Point out every Plasmodium parasite.
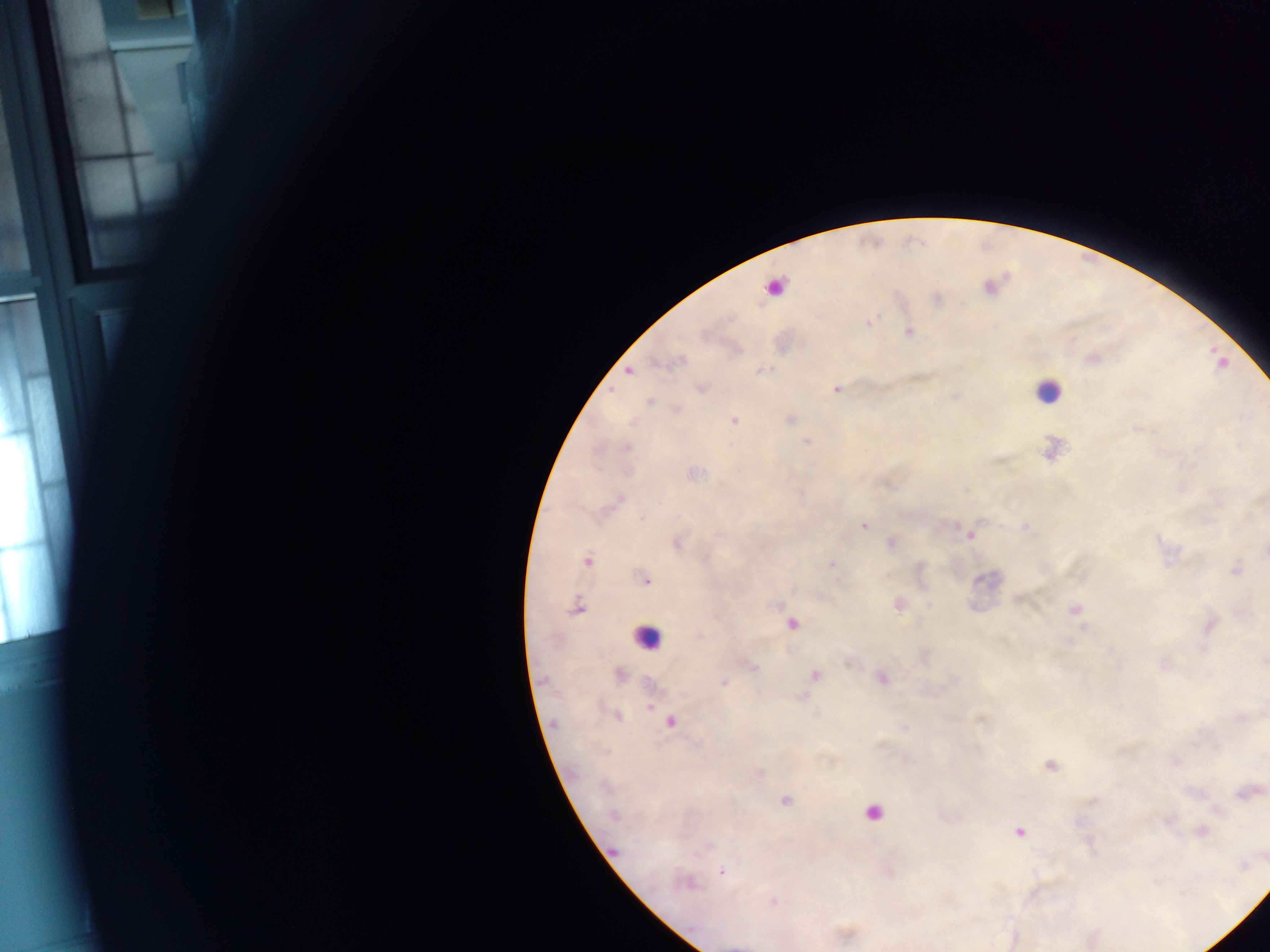
Approximate centers as [x, y] in pixels.
Plasmodium parasites: [989, 287], [936, 299], [868, 322], [909, 331], [1091, 359], [761, 370], [629, 371], [700, 388], [836, 389], [649, 401], [676, 409], [789, 419], [733, 421], [806, 441], [625, 447], [1051, 450], [626, 471], [617, 500], [864, 525], [1026, 527], [970, 534], [677, 542], [891, 543], [587, 561], [832, 566], [919, 568], [1235, 570], [644, 579], [1019, 598], [899, 604], [576, 606], [1074, 609], [791, 623], [1210, 625], [1263, 662], [752, 666], [618, 675], [814, 676], [881, 677], [723, 683], [802, 695], [617, 715], [1241, 718], [670, 721], [1174, 762], [1049, 764], [759, 772], [1246, 793], [785, 799], [614, 815], [1019, 830], [1201, 831], [722, 871], [686, 882], [773, 902], [844, 934].

{
  "country": "Ghana",
  "leukocyte_locations": "approximate centers as [x, y] in pixels: [775, 288], [1047, 390], [646, 637], [872, 812]",
  "capture": "mobile-phone photograph through a microscope",
  "image_size": "1270×952 pixels",
  "field_of_view": "single",
  "preparation": "thick blood film"
}